Report the malaria status of this cell.
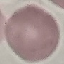

Uninfected.

Cell patch, automatically extracted from a larger field of view and resized to 64 × 64 pixels. Thin blood film. Giemsa stain. Photographed with a smartphone camera at the microscope eyepiece.